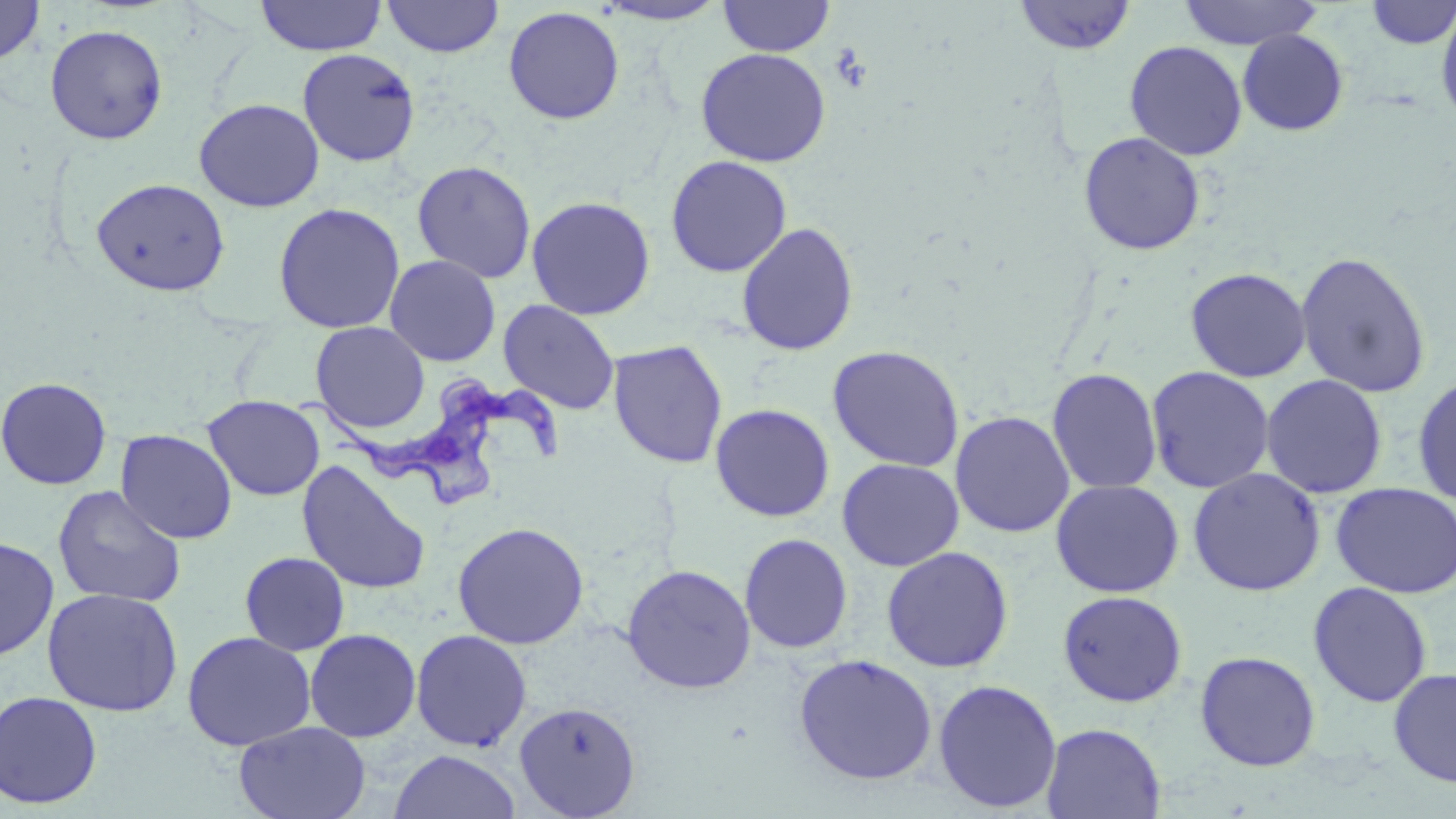
slide-level diagnosis = Trypanosoma brucei
magnification = 1000x
field of view = one of a larger specimen
modality = optical microscopy
image size = 1456×819 pixels
preparation = thin blood smear
uninfected red blood cell locations = approximate bounding boxes as (x1, y1, x2, y2) in pixels: (0, 0, 45, 67), (255, 0, 387, 56), (382, 0, 505, 58), (594, 0, 730, 26), (718, 0, 835, 57), (1012, 0, 1137, 56), (1178, 0, 1324, 50), (1364, 1, 1455, 50), (1435, 3, 1456, 129), (503, 6, 625, 125), (44, 23, 168, 144), (1237, 29, 1349, 136), (1124, 41, 1248, 161), (297, 47, 421, 167), (695, 47, 832, 167), (194, 98, 324, 212), (1078, 131, 1206, 255), (665, 155, 792, 277), (412, 160, 537, 283), (91, 177, 230, 296), (526, 195, 656, 320), (273, 202, 406, 334), (736, 222, 859, 356), (1295, 250, 1432, 398), (385, 254, 501, 366), (1185, 266, 1311, 383), (498, 299, 620, 415), (310, 321, 430, 434), (607, 340, 728, 469), (827, 344, 965, 472), (1145, 365, 1275, 493), (1046, 367, 1163, 495), (1412, 372, 1456, 507), (1260, 373, 1388, 499), (0, 376, 112, 490), (203, 395, 325, 501), (710, 403, 834, 522), (949, 410, 1075, 538), (116, 429, 237, 544), (837, 457, 964, 571), (296, 459, 433, 596), (1187, 467, 1325, 596), (1050, 478, 1185, 598), (1330, 482, 1456, 598), (52, 485, 186, 608), (452, 521, 589, 649), (739, 533, 853, 654), (0, 536, 59, 661), (881, 546, 1013, 673), (239, 551, 350, 656), (621, 563, 757, 693), (1308, 581, 1432, 707), (42, 587, 184, 716), (1057, 590, 1189, 707), (304, 629, 421, 742), (411, 629, 532, 751), (181, 631, 316, 751), (1194, 650, 1321, 772), (794, 654, 938, 786), (1388, 667, 1456, 788), (932, 678, 1062, 813), (0, 691, 103, 810), (514, 701, 641, 817), (234, 721, 371, 819), (1041, 722, 1166, 819), (389, 749, 521, 819)
Trypanosoma brucei locations = approximate bounding boxes as (x1, y1, x2, y2) in pixels: (295, 375, 570, 508)
stain = May-Grünwald-Giemsa